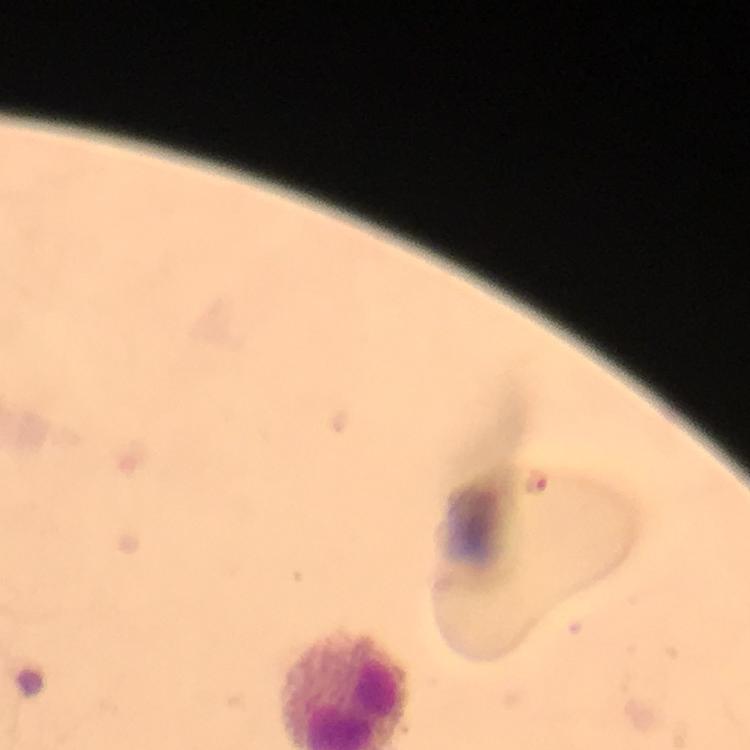

{
  "context": "from a diagnostic examination for malaria",
  "preparation": "thick blood smear",
  "image_size": "750×750 pixels",
  "stain": "Giemsa",
  "immersion_oil": "applied",
  "cropped_from": "one field of view",
  "plasmodium_parasite_locations": "approximate object centers, in pixels from the top-left corner: (x=535, y=481)",
  "magnification": "100x",
  "capture": "smartphone mounted on the microscope"
}